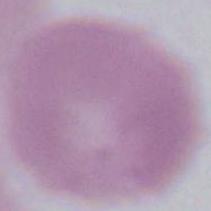
Summary:
  - Magnification: 1000x
  - Identification: red blood cell
  - Modality: micrograph